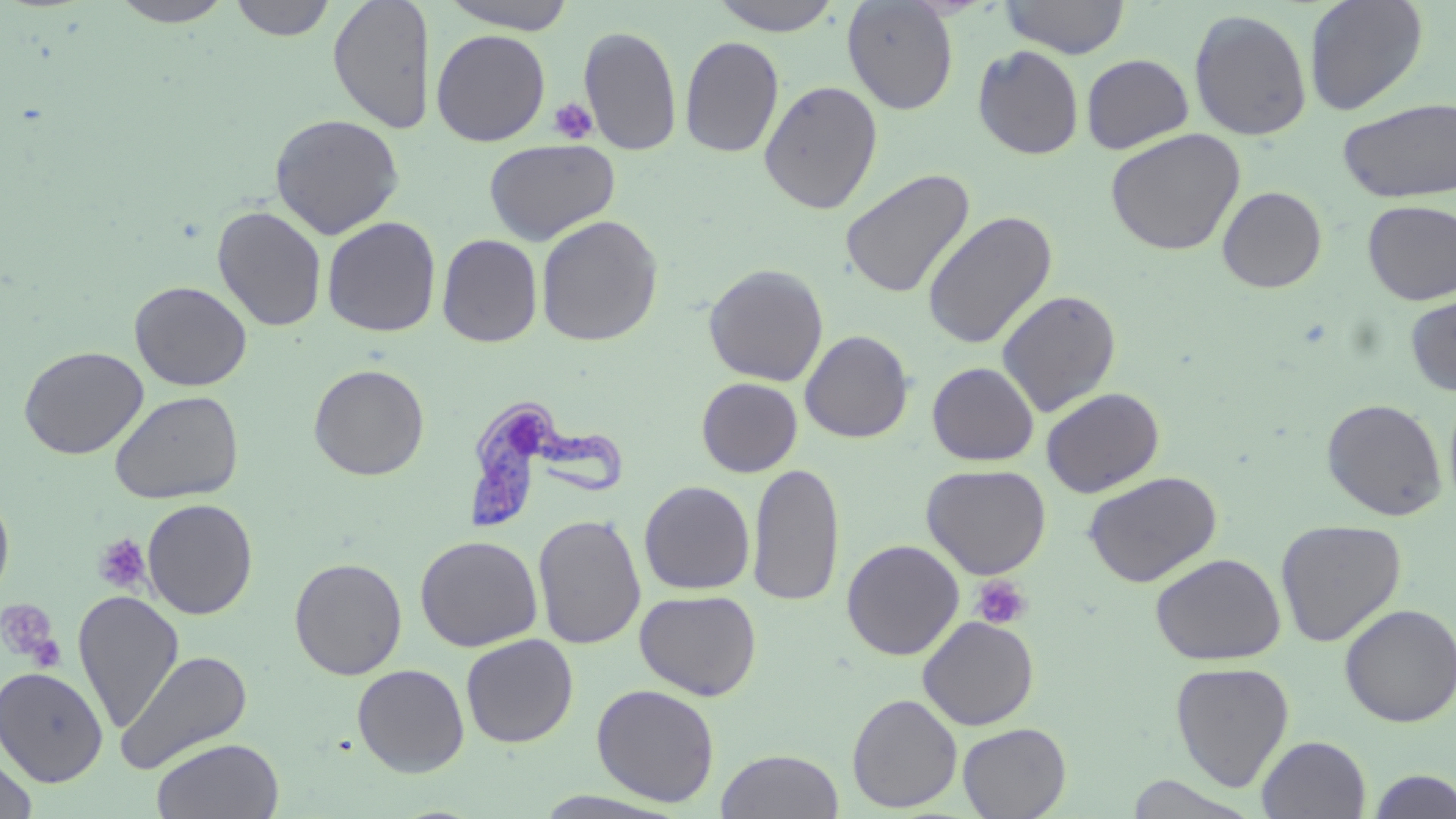

{
  "slide_level_diagnosis": "Trypanosoma brucei",
  "magnification": "1000x",
  "modality": "light microscopy",
  "platelet_locations": "approximate bounding boxes as [x1, y1, x2, y2] in pixels: [549, 98, 598, 145], [92, 533, 150, 594], [971, 575, 1031, 630], [0, 600, 63, 667]",
  "image_size": "1456×819 pixels",
  "field_of_view": "single",
  "preparation": "thin blood smear",
  "uninfected_red_blood_cell_locations": "approximate bounding boxes as [x1, y1, x2, y2] in pixels: [109, 0, 234, 27], [230, 0, 336, 41], [328, 0, 434, 134], [439, 0, 577, 34], [709, 0, 844, 35], [841, 0, 960, 115], [999, 0, 1131, 59], [1304, 0, 1428, 116], [1188, 9, 1313, 142], [578, 25, 682, 156], [431, 29, 550, 146], [679, 36, 784, 158], [972, 45, 1085, 160], [1081, 53, 1194, 155], [758, 80, 883, 215], [1337, 97, 1456, 203], [269, 113, 405, 239], [1105, 128, 1246, 256], [483, 138, 620, 245], [840, 168, 975, 299], [1217, 186, 1327, 293], [1362, 200, 1456, 304], [212, 205, 327, 332], [921, 211, 1058, 350], [535, 215, 663, 347], [321, 216, 441, 337], [437, 234, 543, 348], [703, 263, 829, 386], [130, 280, 252, 391], [996, 289, 1122, 417], [1404, 292, 1456, 397], [800, 330, 914, 443], [18, 345, 149, 460], [927, 362, 1039, 466], [308, 363, 430, 480], [696, 377, 803, 477], [1443, 384, 1456, 513], [1040, 387, 1165, 497], [109, 390, 243, 505], [1321, 398, 1447, 521], [747, 461, 844, 608], [921, 464, 1051, 579], [1083, 471, 1222, 587], [639, 480, 755, 595], [0, 486, 15, 605], [141, 498, 258, 619], [533, 512, 646, 650], [1275, 518, 1407, 647], [415, 535, 542, 652], [842, 539, 964, 661], [1150, 553, 1286, 666], [289, 556, 408, 680], [634, 589, 762, 700], [72, 590, 184, 732], [1339, 603, 1456, 727], [917, 615, 1039, 730], [460, 633, 579, 747], [115, 650, 253, 774], [1170, 661, 1294, 792], [352, 664, 469, 777], [0, 666, 108, 786], [591, 683, 720, 807], [846, 693, 963, 812], [957, 722, 1070, 818], [1256, 735, 1371, 819], [150, 737, 285, 819], [716, 749, 844, 819], [0, 751, 38, 819], [1365, 769, 1456, 818], [1126, 774, 1260, 818]",
  "stain": "May-Grünwald-Giemsa",
  "trypanosoma_brucei_locations": "approximate bounding boxes as [x1, y1, x2, y2] in pixels: [459, 398, 627, 533]"
}